Assess the morphology of the erythrocytes.
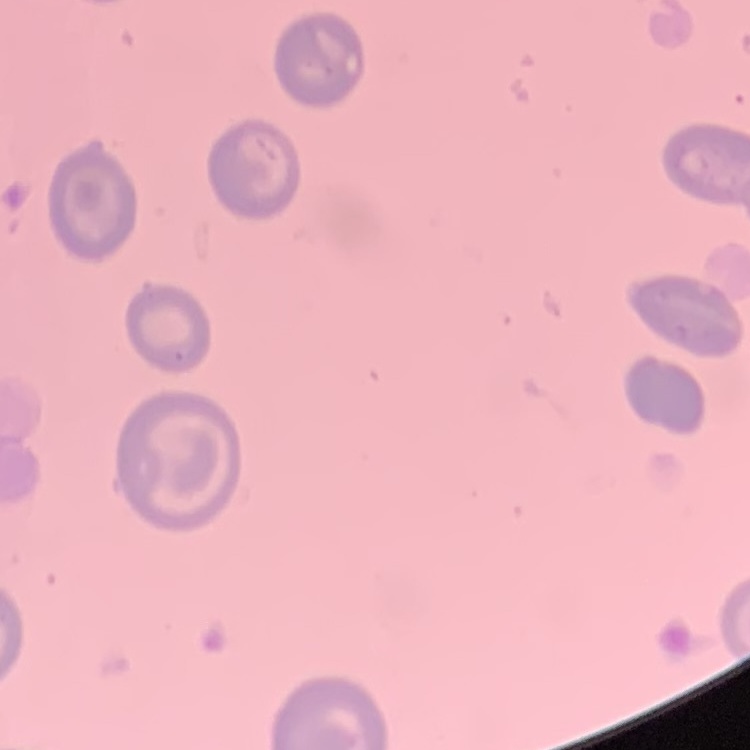
They show no rouleaux formation.

preparation: thin peripheral smear
image_type: one tile cut from a larger photomicrograph
stain: Field's or Giemsa